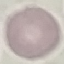

Summary:
  - Malaria status: uninfected
  - Image type: cell patch, automatically extracted from a larger field of view and resized to 64 × 64 pixels
  - Capture: smartphone camera at the microscope eyepiece
  - Preparation: thin smear
  - Stain: Giemsa